Assess the morphology of the erythrocytes.
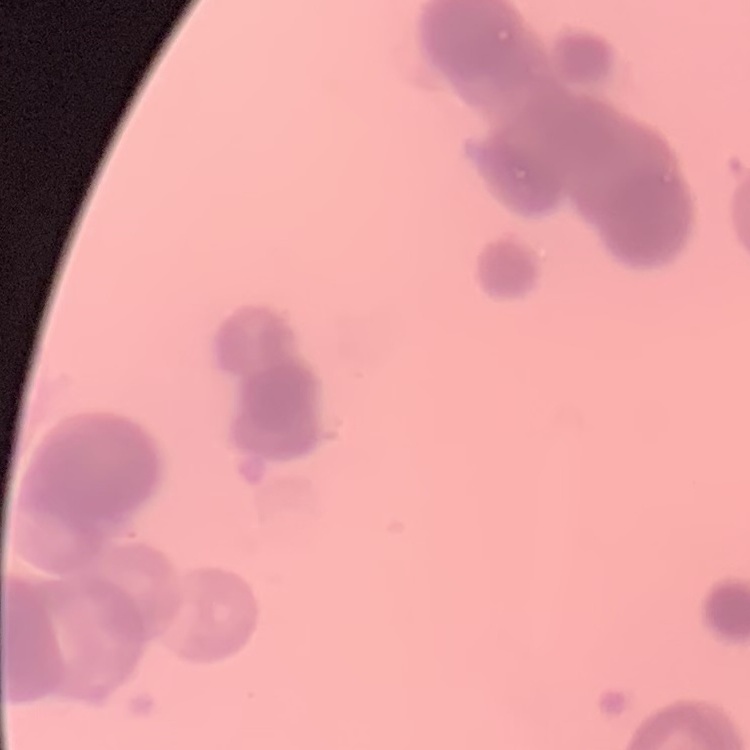

Rouleaux formation.

preparation = thin blood film
image type = one tile cut from a larger photomicrograph
stain = Field's or Giemsa